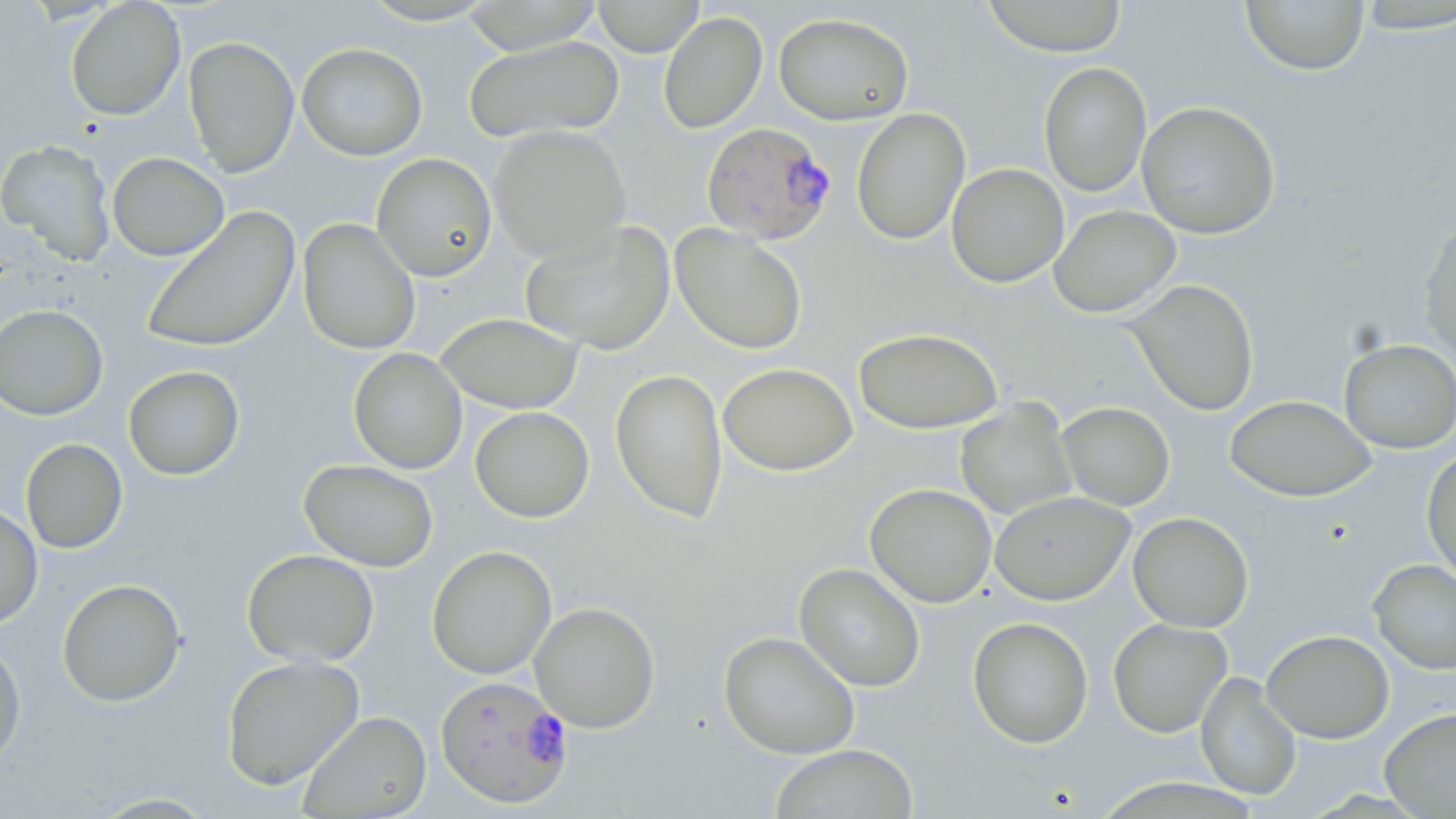
Summary:
  - Coordinate format: approximate bounding boxes as [x1, y1, x2, y2] in pixels
  - Plasmodium falciparum-infected red blood cell locations: [700, 122, 836, 246], [435, 675, 574, 809]
  - Uninfected red blood cell locations: [592, 0, 705, 56], [980, 0, 1128, 57], [1240, 0, 1370, 76], [65, 1, 186, 121], [355, 1, 501, 26], [459, 1, 605, 53], [1351, 1, 1456, 34], [658, 11, 767, 134], [773, 12, 914, 125], [463, 35, 624, 144], [183, 36, 300, 177], [297, 42, 428, 161], [1038, 62, 1152, 197], [1136, 101, 1281, 239], [851, 108, 970, 245], [488, 125, 632, 264], [0, 138, 117, 266], [107, 152, 229, 261], [371, 153, 497, 282], [945, 163, 1069, 288], [1049, 204, 1181, 318], [141, 207, 300, 354], [297, 219, 421, 355], [1418, 219, 1456, 363], [520, 220, 675, 355], [670, 224, 808, 355], [1126, 279, 1260, 416], [0, 303, 109, 421], [435, 313, 583, 414], [852, 327, 1004, 434], [1338, 338, 1456, 454], [348, 347, 468, 475], [718, 362, 857, 476], [123, 365, 245, 481], [610, 368, 728, 525], [1224, 394, 1377, 503], [954, 399, 1077, 519], [1057, 401, 1175, 510], [470, 406, 595, 523], [21, 438, 128, 554], [1421, 448, 1456, 584], [299, 458, 439, 571], [864, 483, 996, 607], [989, 491, 1135, 605], [0, 503, 43, 630], [1128, 512, 1254, 633], [426, 545, 557, 680], [241, 548, 379, 668], [1367, 558, 1456, 674], [794, 562, 925, 692], [56, 578, 187, 707], [529, 601, 661, 733], [967, 616, 1094, 748], [1107, 618, 1232, 737], [1261, 629, 1395, 744], [718, 631, 860, 759], [0, 636, 26, 771], [221, 654, 364, 791], [1195, 671, 1302, 801], [1379, 707, 1456, 818], [298, 710, 432, 818], [769, 744, 918, 819], [86, 791, 223, 818]
  - Slide-level diagnosis: Plasmodium falciparum
  - Stain: May-Grünwald-Giemsa
  - Image size: 1456×819 pixels
  - Preparation: thin blood smear
  - Magnification: 1000x
  - Modality: optical microscopy
  - Field of view: one of a larger specimen